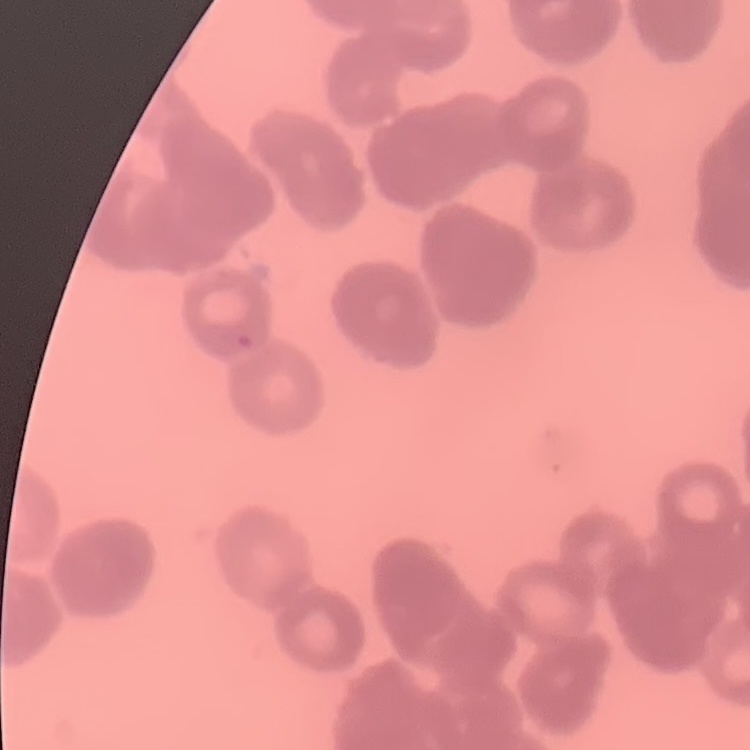

Summary:
  - Red blood cell morphology: rouleaux formation
  - Image type: square crop of a larger photomicrograph
  - Preparation: thin blood film
  - Stain: Field's or Giemsa